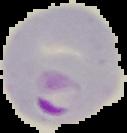

Summary:
  - Preparation: thin blood smear
  - Malaria status: parasitized
  - Image size: 127×133 pixels
  - Image type: cell region segmented out of the field of view; surrounding area masked to black